Locate every malaria parasite.
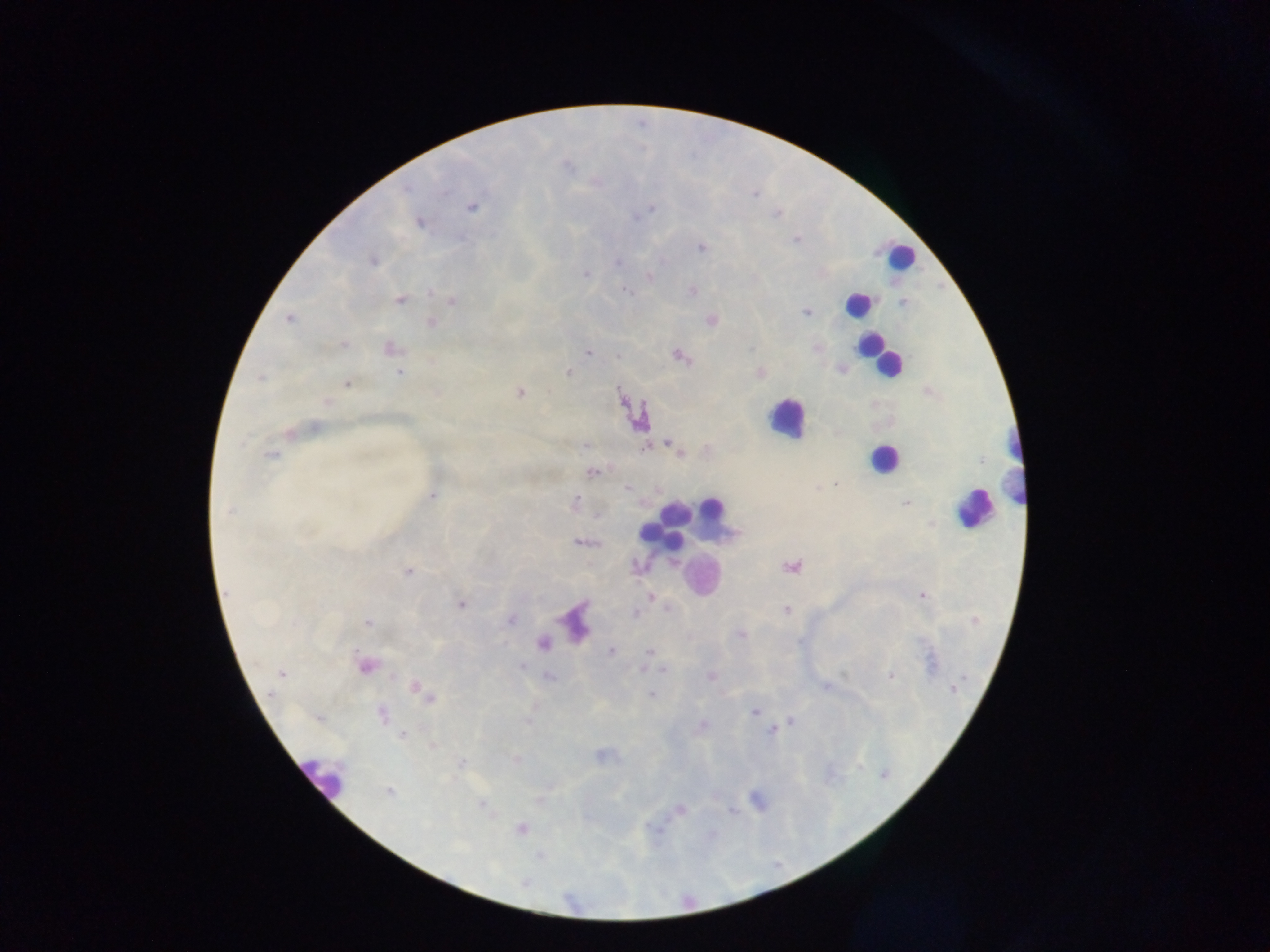
Approximate centers as {x, y} in pixels.
Malaria parasites: {755, 194}, {472, 207}, {651, 209}, {777, 214}, {636, 218}, {419, 222}, {796, 240}, {702, 247}, {372, 262}, {618, 263}, {586, 274}, {649, 277}, {626, 291}, {693, 291}, {432, 292}, {399, 301}, {452, 301}, {806, 312}, {288, 319}, {711, 321}, {432, 322}, {344, 344}, {390, 348}, {751, 348}, {817, 348}, {588, 353}, {618, 355}, {679, 356}, {568, 371}, {399, 372}, {761, 372}, {260, 378}, {346, 383}, {520, 393}, {327, 402}, {316, 427}, {289, 433}, {243, 442}, {586, 445}, {671, 445}, {645, 447}, {707, 448}, {271, 454}, {679, 454}, {593, 472}, {835, 484}, {627, 488}, {433, 496}, {575, 502}, {906, 503}, {229, 510}, {579, 542}, {791, 566}, {637, 568}, {409, 572}, {922, 595}, {651, 596}, {461, 605}, {786, 610}, {636, 613}, {510, 619}, {975, 620}, {368, 622}, {740, 635}, {610, 651}, {648, 653}, {521, 666}, {643, 667}, {664, 670}, {282, 673}, {549, 676}, {711, 676}, {890, 676}, {825, 687}, {417, 688}, {953, 689}, {651, 694}, {426, 696}, {755, 712}, {382, 714}, {791, 721}, {702, 725}, {772, 731}, {402, 734}, {432, 745}, {600, 755}, {517, 760}, {461, 762}, {389, 792}, {482, 804}, {680, 810}, {731, 811}, {521, 829}.

image_size: 1270×952 pixels
preparation: thick blood film
leukocyte_locations: 'approximate centers as {x, y} in pixels: {899, 256}, {857, 305}, {877, 355}, {786, 418}, {883, 458}, {1010, 464}, {974, 508}, {712, 509}, {674, 512}, {651, 533}, {671, 536}, {700, 574}, {576, 616}, {546, 640}, {370, 665}, {321, 775}'
country: Ghana
field_of_view: single
capture: mobile-phone photograph through a microscope